Assess this cell for malaria.
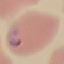
Parasitized.

capture = smartphone through the microscope eyepiece
preparation = thin blood smear
image type = automatically extracted cell patch, resized to 64 × 64 pixels
stain = Giemsa